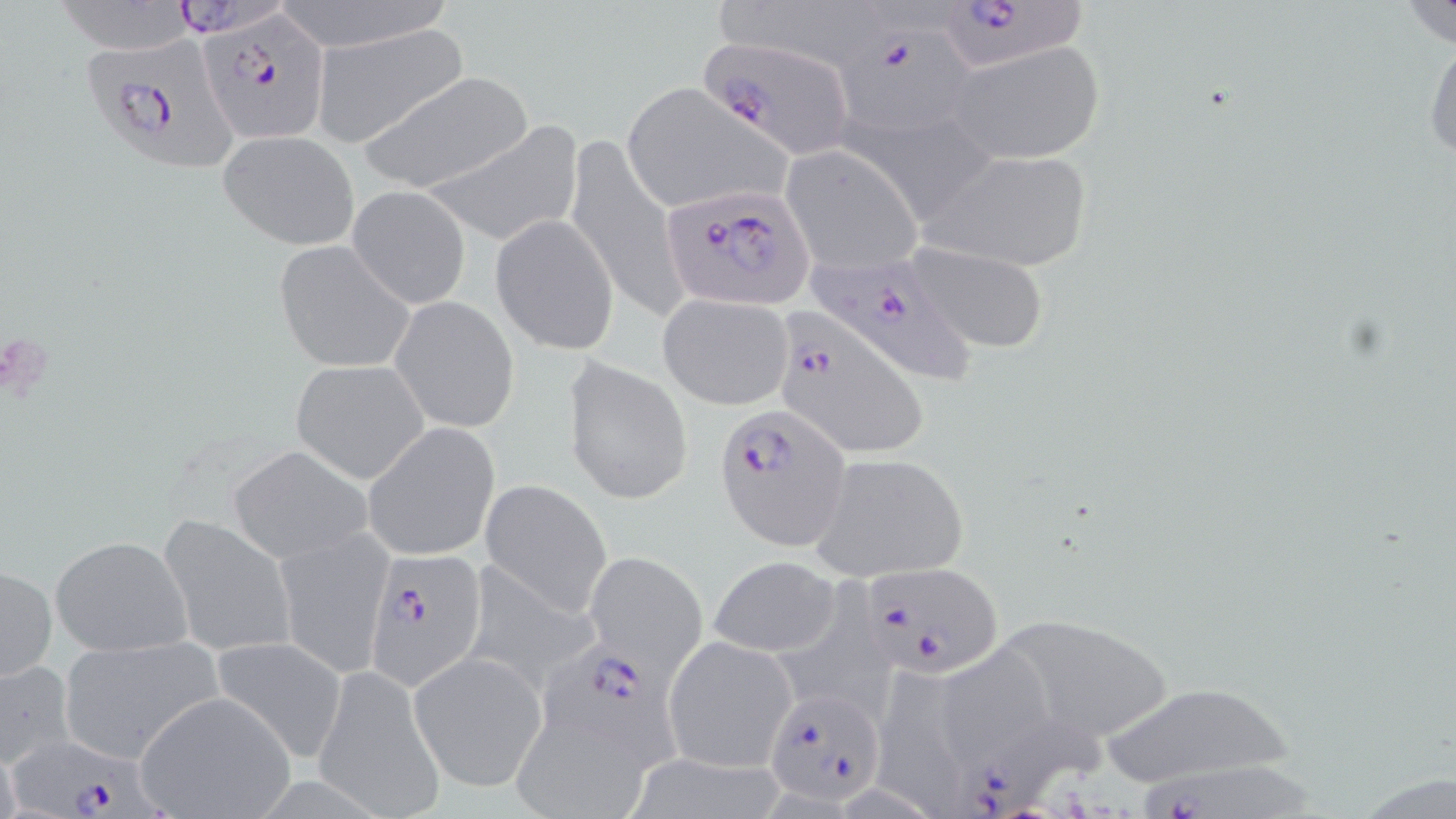
{
  "slide_level_diagnosis": "Plasmodium falciparum",
  "field_of_view": "single",
  "uninfected_red_blood_cell_locations": "approximate bounding boxes as (x1,y1)-(x2,y2) corner pairs in pixels: (269,1)-(456,53), (1399,1)-(1456,50), (311,23)-(470,149), (1424,30)-(1456,169), (944,38)-(1106,165), (356,69)-(537,194), (618,82)-(793,216), (842,107)-(996,221), (419,121)-(583,246), (218,129)-(360,250), (563,131)-(688,325), (782,146)-(923,273), (920,149)-(1096,274), (347,185)-(471,310), (489,214)-(619,354), (273,240)-(415,373), (899,241)-(1053,354), (658,293)-(794,412), (389,295)-(520,433), (563,358)-(693,504), (290,360)-(429,483), (363,423)-(500,561), (229,447)-(374,565), (810,452)-(970,582), (481,478)-(612,617), (158,516)-(297,658), (273,528)-(392,677), (50,534)-(194,657), (584,552)-(706,679), (707,555)-(842,658), (1,562)-(56,684), (461,562)-(601,696), (783,563)-(900,709), (989,611)-(1176,742), (55,634)-(223,764), (664,634)-(798,773), (209,637)-(350,763), (409,653)-(546,791), (0,657)-(78,769), (312,665)-(446,819), (883,673)-(969,814), (1095,680)-(1299,788), (133,691)-(297,818), (504,719)-(649,819)",
  "preparation": "thin blood smear",
  "image_size": "1456×819 pixels",
  "magnification": "1000x",
  "plasmodium_falciparum_infected_red_blood_cell_locations": "approximate bounding boxes as (x1,y1)-(x2,y2) corner pairs in pixels: (53,0)-(214,54), (920,0)-(1095,78), (200,11)-(332,144), (839,25)-(985,131), (696,33)-(857,157), (83,36)-(241,176), (659,185)-(816,311), (805,250)-(981,383), (771,306)-(929,459), (716,404)-(849,550), (364,550)-(490,688), (855,563)-(1001,678), (530,641)-(674,776), (762,686)-(885,804), (961,721)-(1107,815), (11,737)-(162,819), (1126,763)-(1333,819)",
  "stain": "May-Grünwald-Giemsa",
  "modality": "optical microscopy"
}